Assess this cell for malaria.
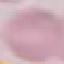

It is uninfected.

Photographed with a smartphone camera at the microscope eyepiece. Giemsa-stained preparation. Thin blood film. Cell patch, automatically extracted from a larger field of view and resized to 64 × 64 pixels.